State which cell type is depicted.
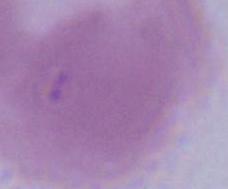
This is an erythrocyte.

modality = photomicrograph
magnification = 1000x